Report the malaria status of this cell.
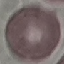
It is uninfected.

capture = smartphone camera at the microscope eyepiece
image type = automatically extracted cell patch, resized to 64 × 64 pixels
preparation = thin blood film
stain = Giemsa